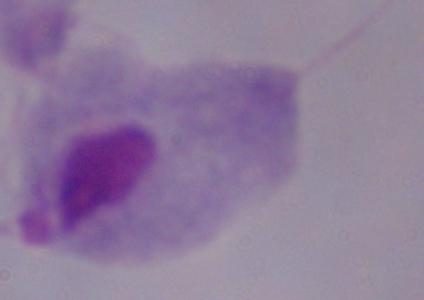
A trichomonad is seen. 1000x magnification. Photomicrograph.